Identify the parasite.
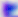
This is Toxoplasma gondii.

Micrograph. Captured at 400x magnification.